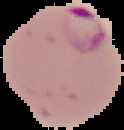

From a thin blood film. Result: malaria parasites identified. Cell region segmented out of the field of view; the surrounding area is masked to black. Image is 124×130 pixels.